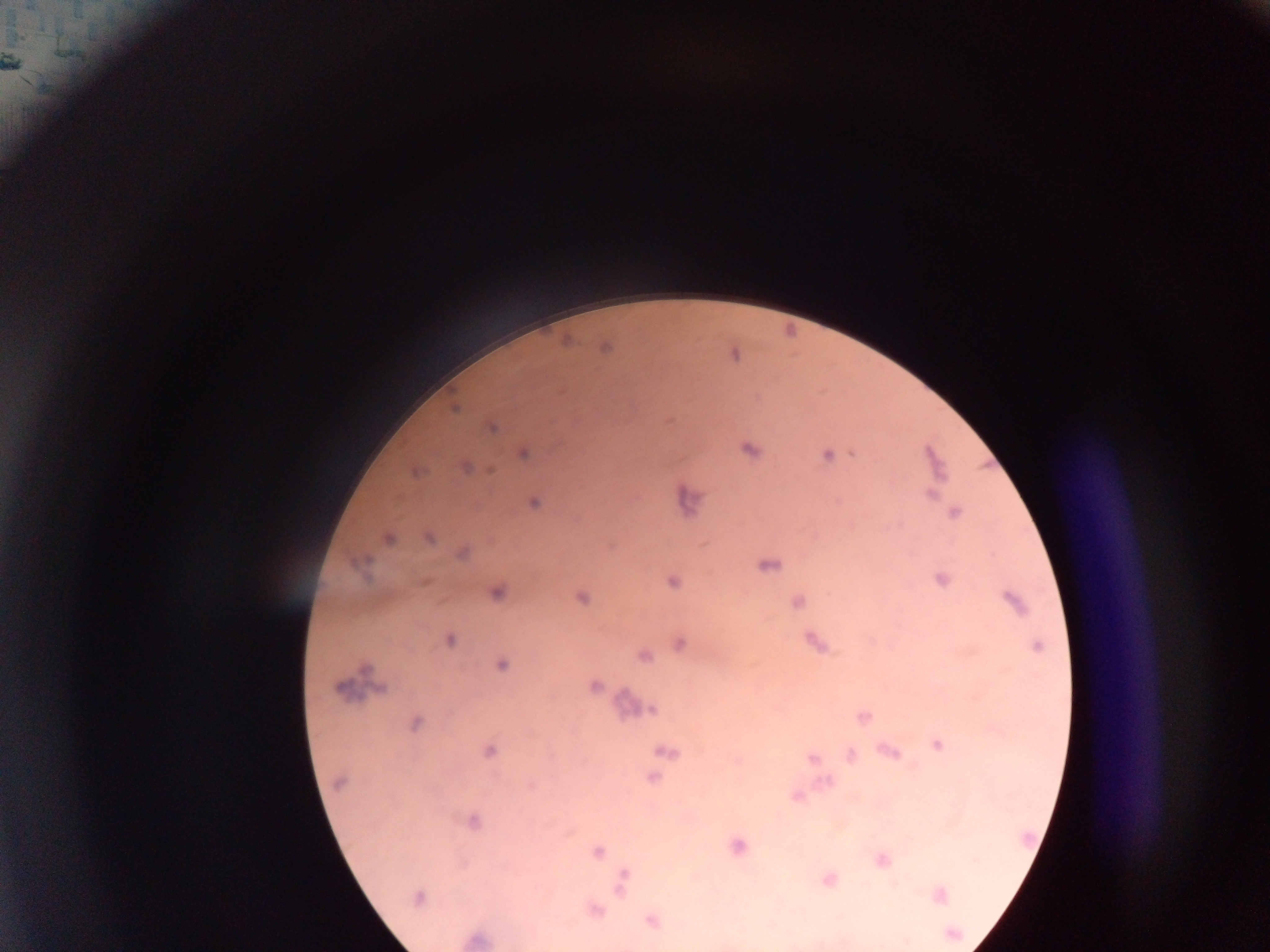

Approximate centers as (x, y) in pixels. Plasmodium parasite locations: (17, 62), (455, 409), (668, 421), (490, 426), (746, 449), (853, 452), (523, 453), (826, 454), (468, 466), (488, 470), (417, 471), (931, 492), (533, 501), (955, 512), (388, 537), (428, 538), (762, 566), (942, 580), (671, 581), (425, 582), (496, 593), (581, 597), (797, 602), (810, 640), (680, 642), (642, 656), (501, 665), (593, 685), (383, 688), (340, 689), (625, 701), (652, 710), (862, 717), (416, 722), (937, 744), (880, 750), (489, 751), (891, 751), (662, 752), (849, 755), (811, 757), (736, 759), (652, 779), (827, 781), (337, 784), (531, 787), (796, 796), (475, 820), (569, 832), (736, 847), (597, 851), (881, 861), (827, 879), (620, 890), (939, 895), (418, 898), (594, 909), (652, 922). Photographed through a microscope with a mobile-phone camera. Single field of view. Collected in Ghana. Thick blood smear. Image is 1270×952 pixels.